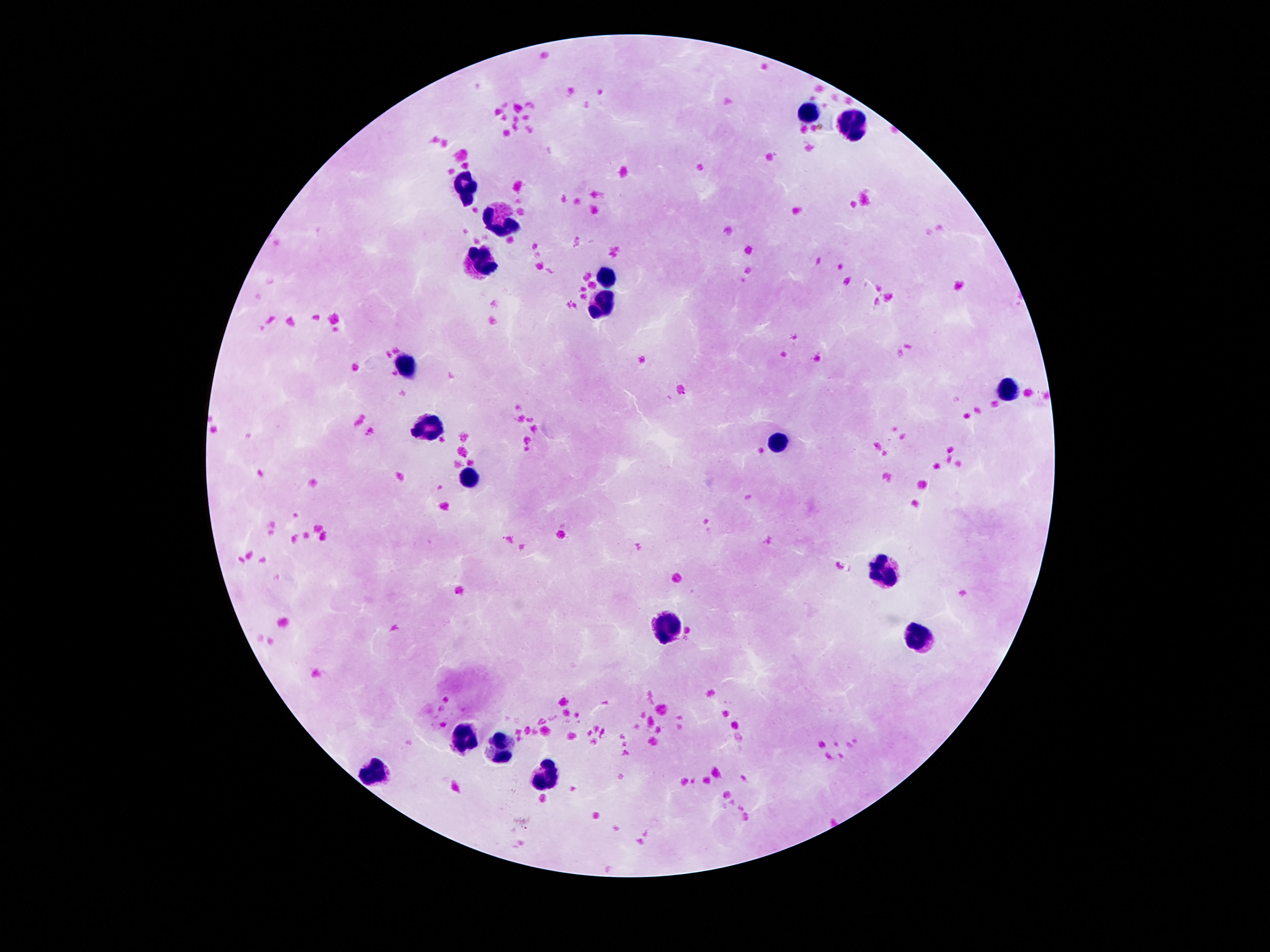
Approximate centers as {x, y} in pixels.
Summary:
  - Leukocyte locations: {809, 110}, {850, 128}, {466, 186}, {503, 222}, {485, 259}, {608, 276}, {604, 304}, {408, 365}, {1007, 388}, {427, 425}, {781, 442}, {468, 478}, {888, 572}, {669, 629}, {921, 634}, {460, 736}, {496, 746}, {548, 771}, {376, 775}
  - Magnification: 100x
  - Capture: smartphone camera through the microscope eyepiece
  - Patient malaria status: negative
  - Image size: 1270×952 pixels
  - Field of view: one from this slide
  - Stain: Giemsa
  - Preparation: thick peripheral-blood smear